Assess the morphology of the red blood cells.
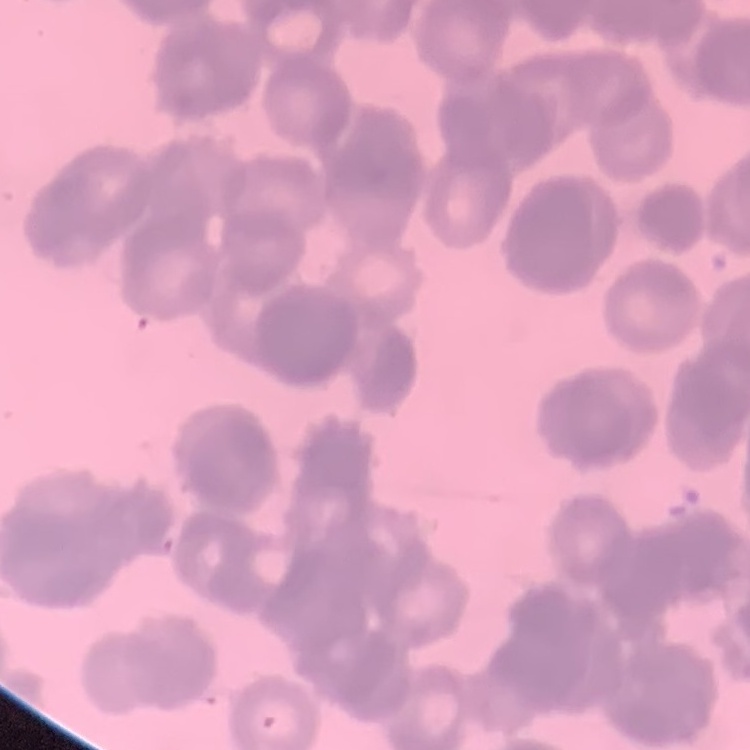
Rouleaux formation.

Thin blood film. Square crop of a larger photomicrograph. Field's or Giemsa stain.